Assess the morphology of the erythrocytes.
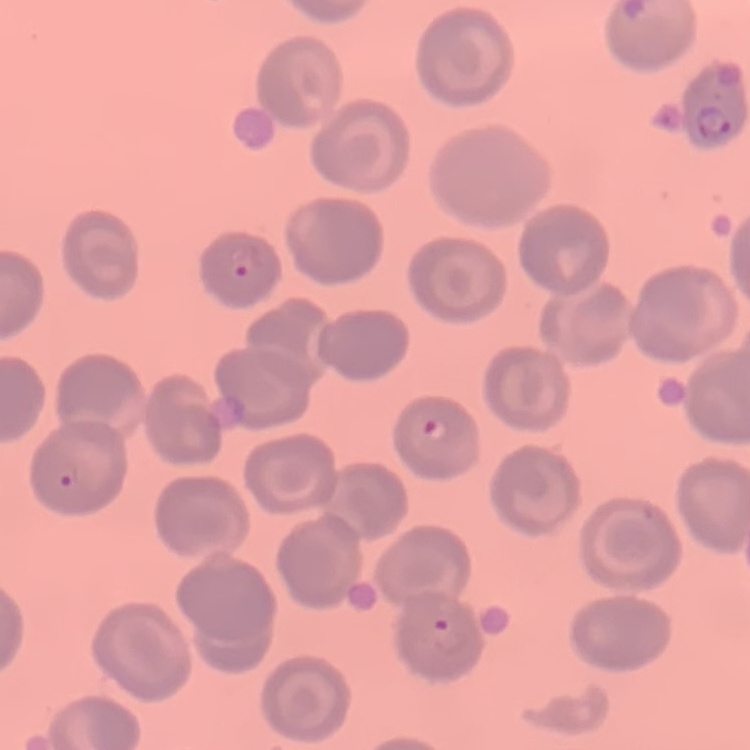

No rouleaux formation.

Summary:
  - Stain: Field's or Giemsa
  - Image type: one tile cut from a larger photomicrograph
  - Preparation: thin blood film